Assess the morphology of the red blood cells.
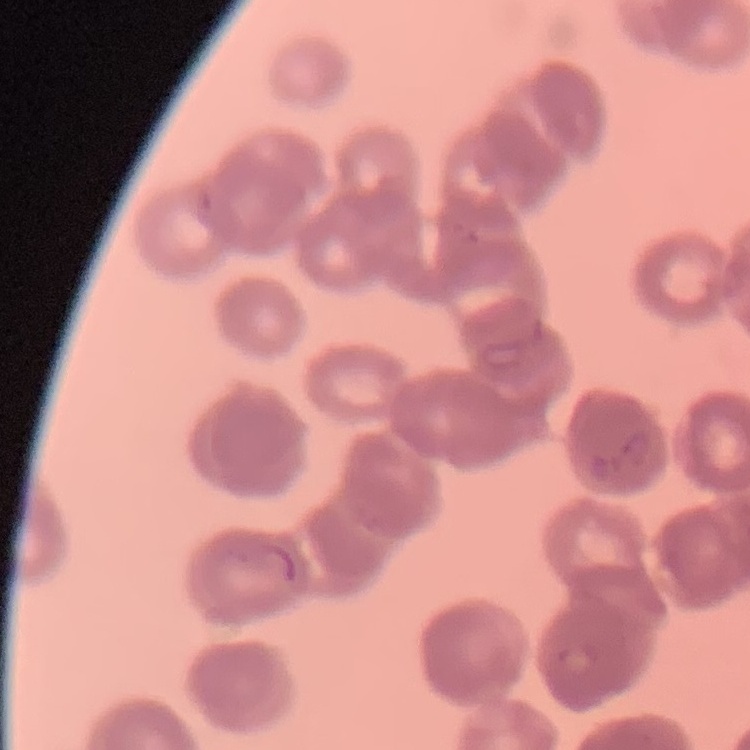
Rouleaux formation.

Summary:
  - Image type: square crop of a larger photomicrograph
  - Preparation: thin peripheral smear
  - Stain: Field's or Giemsa